State which parasite is depicted.
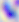
Toxoplasma gondii.

400x magnification. Photomicrograph.